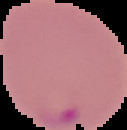

The area outside the segmented cell region is set to black. From a thin blood film. Image is 127×130 pixels. Result: Plasmodium parasites identified.